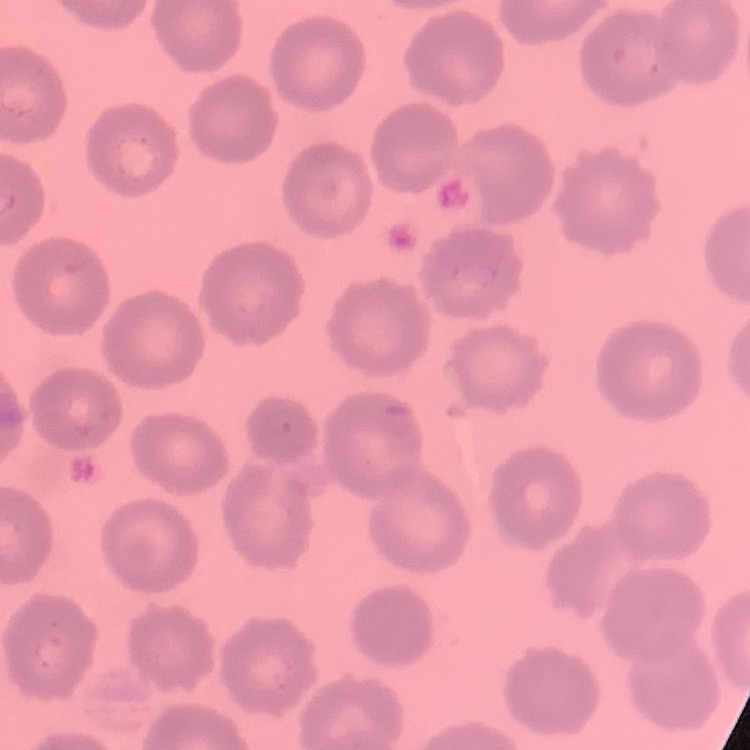
erythrocyte_morphology: no rouleaux formation
preparation: thin blood smear
stain: Field's or Giemsa
image_type: one tile cut from a larger photomicrograph